Look for Plasmodium parasites.
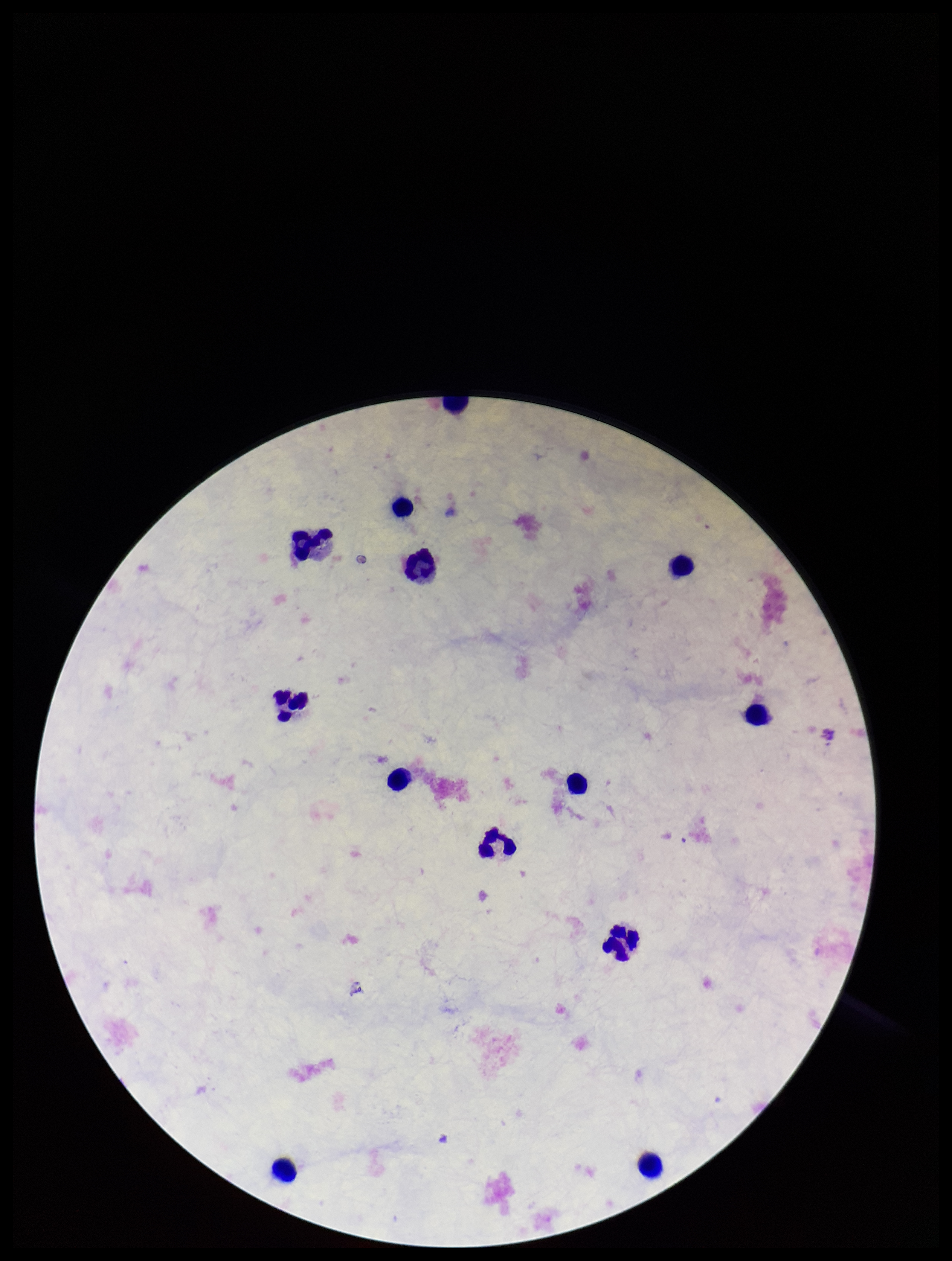

None detected.

{
  "image_size": "952×1261 pixels",
  "capture": "smartphone photograph through the microscope eyepiece",
  "patient_malaria_status": "negative",
  "stain": "Giemsa",
  "leukocyte_count": 13,
  "parasite_count": 0,
  "preparation": "thick smear",
  "field_of_view": "one from this slide"
}